Give the position of every Plasmodium parasite.
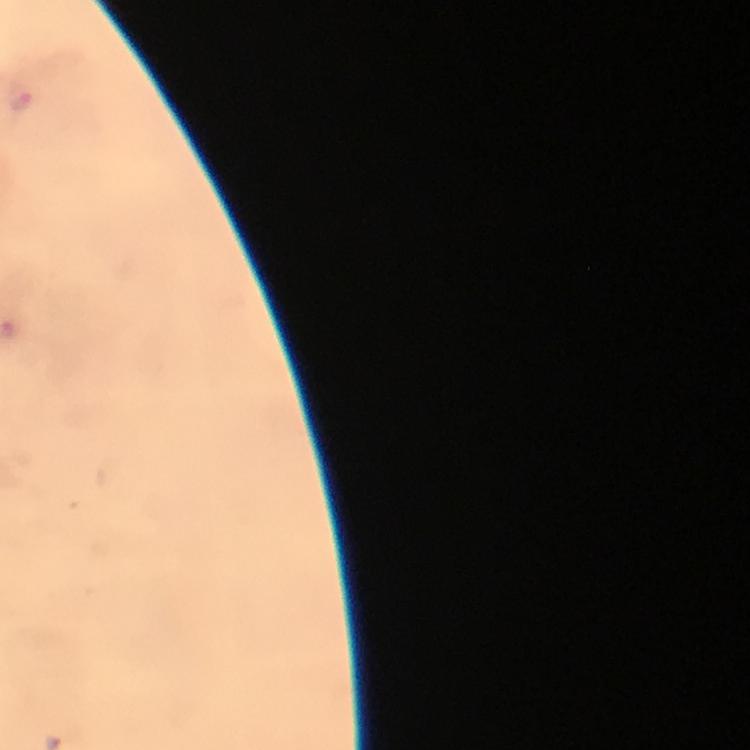

Approximate centers as {x, y} in pixels.
Plasmodium parasites: {22, 98}.

Summary:
  - Immersion oil: used
  - Cropped from: one field of view
  - Image size: 750×750 pixels
  - Preparation: thick smear
  - Capture: smartphone camera through the microscope
  - Context: from a diagnostic examination for malaria
  - Magnification: 100x
  - Stain: Giemsa